Name the parasite shown.
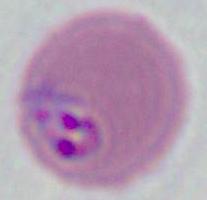
This is Plasmodium.

{
  "modality": "micrograph",
  "magnification": "400x or 1000x"
}